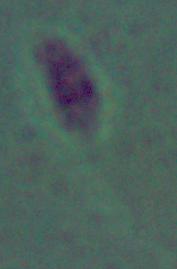

magnification: 1000x
identification: Leishmania
modality: micrograph